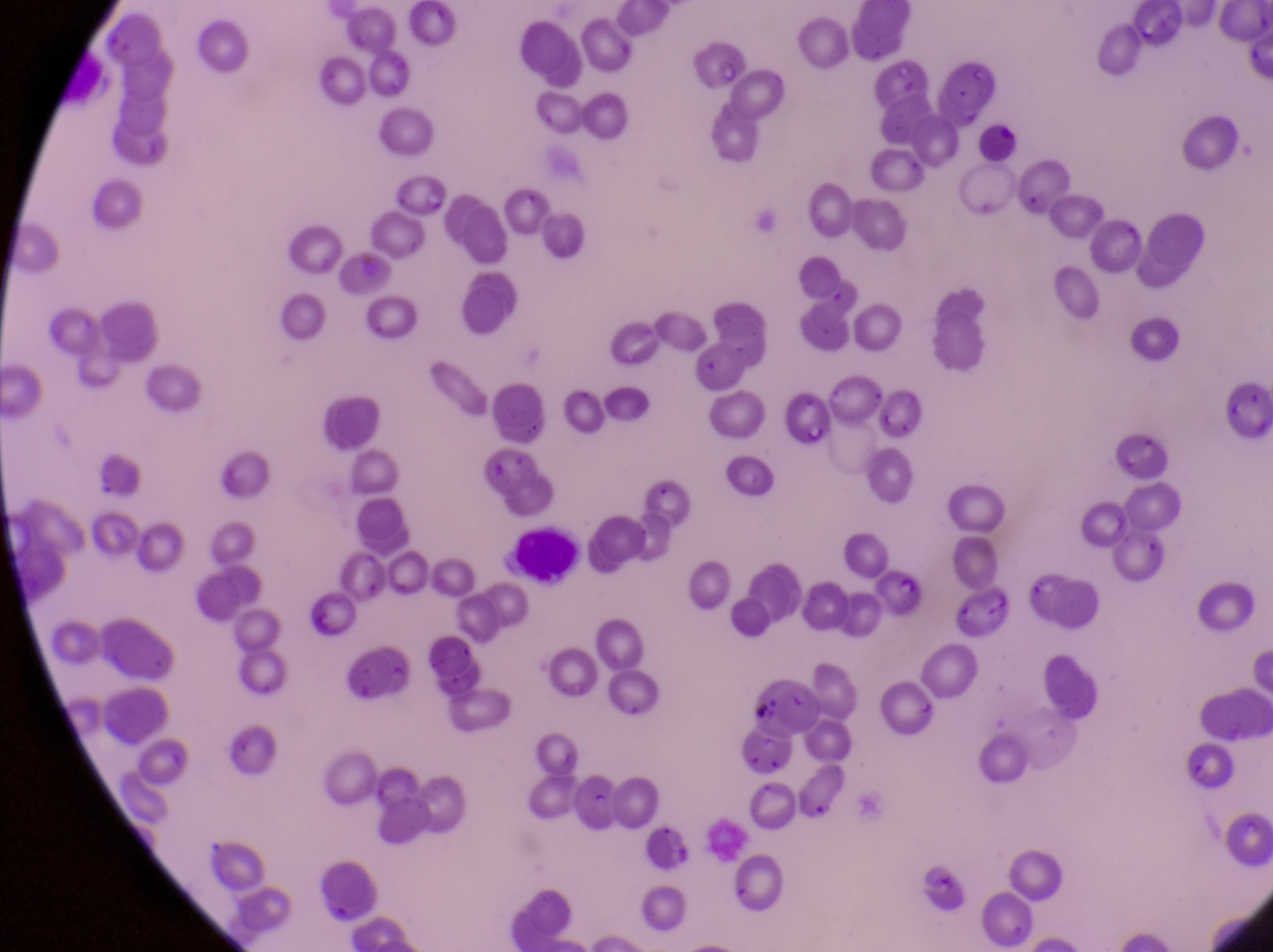

Approximate bounding boxes as {left, top, right, bottom} in pixels.
Summary:
  - Parasitised red blood cell locations: {387, 162, 444, 215}, {779, 392, 846, 464}, {1113, 422, 1178, 484}, {878, 567, 931, 619}, {746, 681, 824, 743}
  - Leukocyte locations: {976, 115, 1021, 167}, {514, 524, 584, 586}
  - Country: Uganda
  - Capture: smartphone photograph through the eyepiece of an Olympus CX-23 microscope
  - Magnification: 1000x
  - Field of view: single
  - Preparation: thin blood smear
  - Image size: 1273×952 pixels